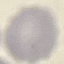

Summary:
  - Malaria status: uninfected
  - Preparation: thin blood smear
  - Image type: automatically extracted cell patch, resized to 64 × 64 pixels
  - Stain: Giemsa
  - Capture: smartphone camera at the microscope eyepiece